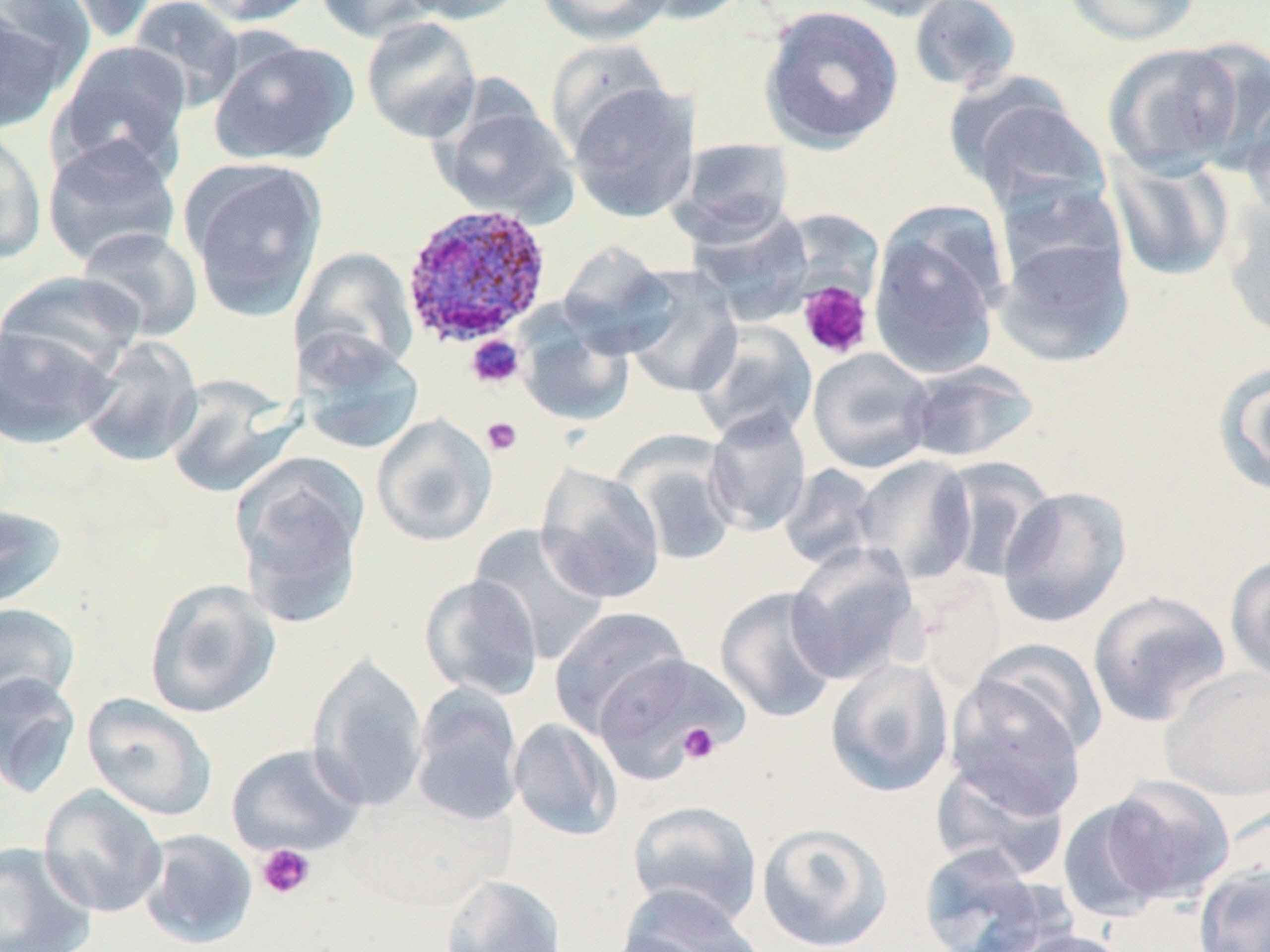

Approximate bounding boxes as (x1, y1, x2, y2) in pixels. Plasmodium ovale-infected red blood cell locations: (400, 203, 553, 349). Platelet locations: (797, 281, 874, 360), (465, 335, 525, 389), (481, 416, 523, 456), (677, 723, 722, 764), (256, 843, 315, 900). Uninfected red blood cell locations: (40, 0, 163, 44), (126, 0, 245, 111), (190, 0, 320, 27), (314, 0, 436, 42), (398, 0, 529, 25), (537, 0, 672, 45), (627, 0, 754, 25), (832, 0, 964, 21), (908, 0, 1022, 93), (1059, 0, 1201, 45), (0, 5, 73, 134), (759, 5, 904, 152), (360, 16, 482, 144), (207, 36, 357, 166), (546, 39, 671, 152), (1179, 39, 1270, 173), (51, 40, 194, 180), (1102, 43, 1248, 177), (567, 82, 698, 223), (954, 84, 1112, 216), (1239, 97, 1270, 228), (434, 99, 576, 221), (0, 126, 48, 264), (41, 134, 183, 269), (671, 138, 795, 244), (1107, 153, 1235, 282), (183, 159, 328, 320), (994, 178, 1128, 291), (1219, 198, 1270, 341), (686, 206, 816, 325), (868, 207, 1008, 380), (76, 226, 204, 343), (992, 234, 1135, 367), (557, 242, 677, 356), (289, 246, 419, 379), (620, 266, 743, 398), (0, 270, 146, 378), (516, 311, 635, 427), (0, 321, 118, 449), (690, 322, 818, 445), (293, 332, 425, 455), (76, 337, 203, 468), (807, 348, 936, 474), (903, 360, 1040, 463), (1214, 362, 1270, 497), (163, 376, 298, 498), (703, 409, 812, 536), (372, 414, 497, 547), (617, 436, 741, 567), (853, 454, 978, 584), (231, 456, 369, 627), (935, 456, 1058, 583), (535, 464, 666, 604), (778, 464, 883, 571), (997, 486, 1132, 628), (0, 503, 68, 612), (469, 524, 611, 664), (785, 543, 922, 685), (1225, 554, 1270, 684), (419, 575, 544, 700), (143, 579, 280, 719), (715, 586, 841, 723), (1087, 590, 1232, 728), (0, 603, 80, 711), (549, 607, 690, 737), (968, 640, 1108, 762), (592, 652, 747, 780), (308, 654, 429, 813), (825, 656, 955, 798), (1159, 666, 1270, 801), (0, 672, 81, 799), (630, 678, 728, 768), (943, 678, 1088, 818), (409, 684, 524, 826), (82, 693, 217, 821), (509, 718, 622, 841), (226, 743, 366, 857), (930, 758, 1071, 880), (1100, 774, 1239, 906), (38, 785, 168, 918), (1058, 797, 1175, 923), (627, 799, 762, 927), (756, 821, 893, 951), (138, 829, 258, 949), (0, 841, 97, 951), (916, 844, 1060, 952), (1193, 864, 1270, 952), (440, 873, 569, 952), (614, 887, 767, 952), (1001, 929, 1137, 952). Slide-level diagnosis: Plasmodium ovale. Single field of view. May-Grünwald-Giemsa stain. Light microscopy. 1000x magnification. Image is 1270×952 pixels. Thin blood smear.